Outline each blood parasite and name the species.
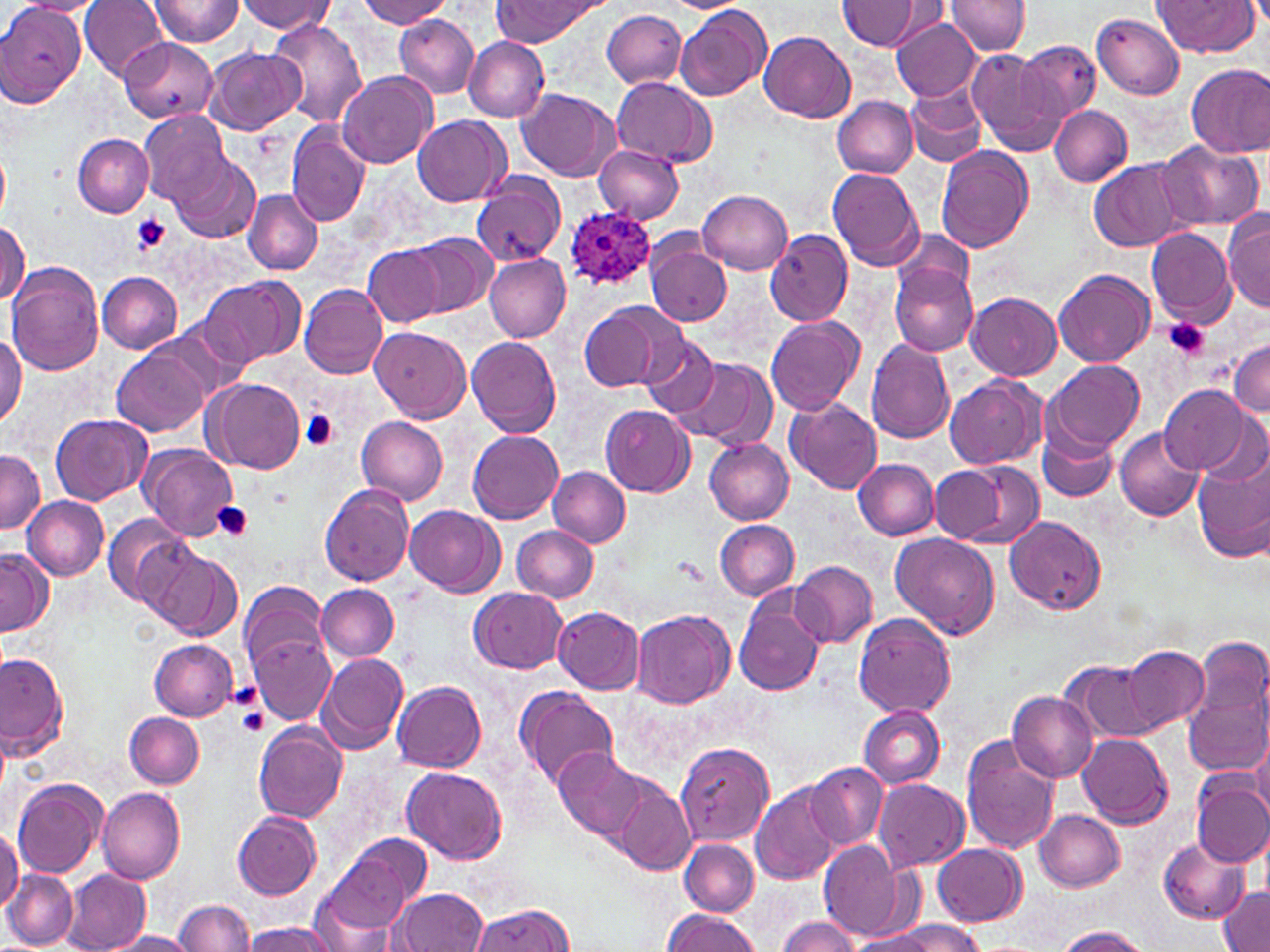
Approximate bounding boxes as (x1, y1, x2, y2) in pixels.
Plasmodium ovale-infected red blood cells: (565, 208, 656, 290).
No Plasmodium falciparum, Plasmodium malariae, Plasmodium vivax, Babesia divergens, or Trypanosoma brucei observed.

Platelet locations: (129, 214, 169, 255), (1164, 317, 1209, 361), (299, 409, 341, 451), (213, 502, 253, 539), (237, 705, 270, 735). Uninfected red blood cell locations: (147, 0, 246, 48), (355, 0, 451, 27), (493, 0, 602, 43), (946, 0, 1033, 55), (11, 1, 105, 18), (80, 1, 167, 80), (238, 1, 335, 34), (838, 1, 921, 50), (1152, 1, 1257, 56), (0, 2, 86, 107), (676, 5, 771, 101), (602, 9, 687, 89), (1093, 13, 1185, 99), (395, 15, 480, 98), (890, 16, 982, 101), (267, 18, 368, 128), (758, 31, 855, 120), (463, 37, 549, 120), (119, 38, 218, 126), (1015, 39, 1101, 126), (205, 45, 304, 134), (968, 47, 1061, 148), (1185, 63, 1270, 157), (339, 71, 437, 169), (611, 77, 714, 165), (905, 87, 987, 167), (518, 89, 619, 181), (833, 97, 919, 178), (1050, 105, 1131, 187), (138, 109, 227, 206), (413, 115, 510, 206), (286, 124, 371, 228), (73, 134, 153, 216), (1153, 140, 1264, 232), (594, 144, 683, 223), (935, 145, 1035, 253), (0, 147, 11, 221), (167, 151, 261, 244), (1089, 159, 1183, 253), (826, 167, 924, 271), (472, 171, 565, 268), (242, 189, 322, 275), (697, 189, 792, 274), (1223, 210, 1270, 313), (0, 219, 29, 305), (894, 227, 973, 297), (1145, 228, 1236, 326), (763, 229, 852, 326), (409, 233, 494, 316), (645, 239, 733, 328), (362, 245, 444, 326), (484, 253, 572, 342), (888, 261, 978, 357), (7, 262, 104, 375), (1053, 268, 1156, 367), (97, 272, 182, 353), (197, 276, 302, 370), (300, 284, 387, 379), (967, 292, 1061, 380), (581, 300, 686, 394), (766, 316, 865, 415), (370, 326, 471, 423), (0, 329, 26, 428), (637, 334, 723, 420), (467, 337, 562, 438), (1230, 338, 1270, 417), (866, 339, 955, 444), (112, 346, 209, 438), (670, 359, 773, 448), (1045, 360, 1143, 453), (944, 375, 1044, 470), (206, 377, 305, 474), (1159, 384, 1249, 473), (787, 398, 882, 496), (600, 405, 694, 497), (51, 414, 152, 506), (358, 417, 447, 504), (1038, 422, 1118, 504), (1114, 428, 1204, 521), (468, 430, 563, 524), (705, 438, 794, 524), (140, 444, 239, 541), (1192, 444, 1270, 562), (0, 449, 44, 535), (853, 458, 940, 540), (937, 461, 1045, 550), (548, 467, 630, 548), (320, 484, 416, 586), (23, 495, 109, 580), (405, 505, 501, 596), (102, 513, 194, 609), (1005, 515, 1106, 614), (715, 520, 799, 601), (511, 524, 599, 602), (891, 531, 1000, 639), (0, 548, 52, 637), (148, 550, 242, 640), (790, 561, 877, 649), (240, 580, 327, 673), (316, 585, 399, 660), (468, 587, 568, 673), (733, 590, 826, 696), (553, 607, 644, 694), (632, 608, 735, 708), (854, 614, 956, 717), (251, 634, 336, 723), (1194, 635, 1268, 721), (149, 638, 238, 720), (1122, 646, 1206, 730), (0, 651, 69, 761), (317, 653, 406, 753), (1065, 661, 1160, 743), (392, 681, 486, 772), (515, 685, 620, 792), (1008, 691, 1098, 783), (1185, 691, 1269, 778), (859, 706, 944, 788), (125, 712, 204, 788), (0, 722, 13, 797), (254, 723, 347, 822), (1078, 733, 1173, 828), (962, 736, 1059, 854), (1248, 736, 1270, 820), (674, 740, 774, 847), (553, 747, 651, 843), (805, 761, 887, 848), (402, 765, 508, 863), (1191, 777, 1270, 867), (871, 778, 970, 872), (13, 779, 105, 879), (613, 780, 695, 876), (750, 783, 842, 884), (97, 787, 185, 884), (1035, 809, 1125, 892), (232, 811, 322, 900), (0, 826, 22, 912), (320, 836, 431, 940), (679, 839, 759, 915), (1159, 839, 1250, 922), (819, 840, 910, 942), (932, 843, 1025, 925), (4, 869, 79, 949), (62, 870, 150, 951), (393, 888, 488, 952), (1219, 889, 1270, 951), (175, 899, 253, 951), (469, 902, 577, 951), (661, 909, 760, 951), (777, 916, 862, 952), (884, 920, 985, 952), (245, 922, 338, 952), (1055, 927, 1149, 952), (848, 930, 939, 951), (102, 931, 201, 951). Slide-level diagnosis: Plasmodium ovale. Thin blood film. Single field of view. May-Grünwald-Giemsa-stained preparation. Captured at 1000x magnification. Image is 1270×952 pixels. Optical microscopy.